State the preparation type.
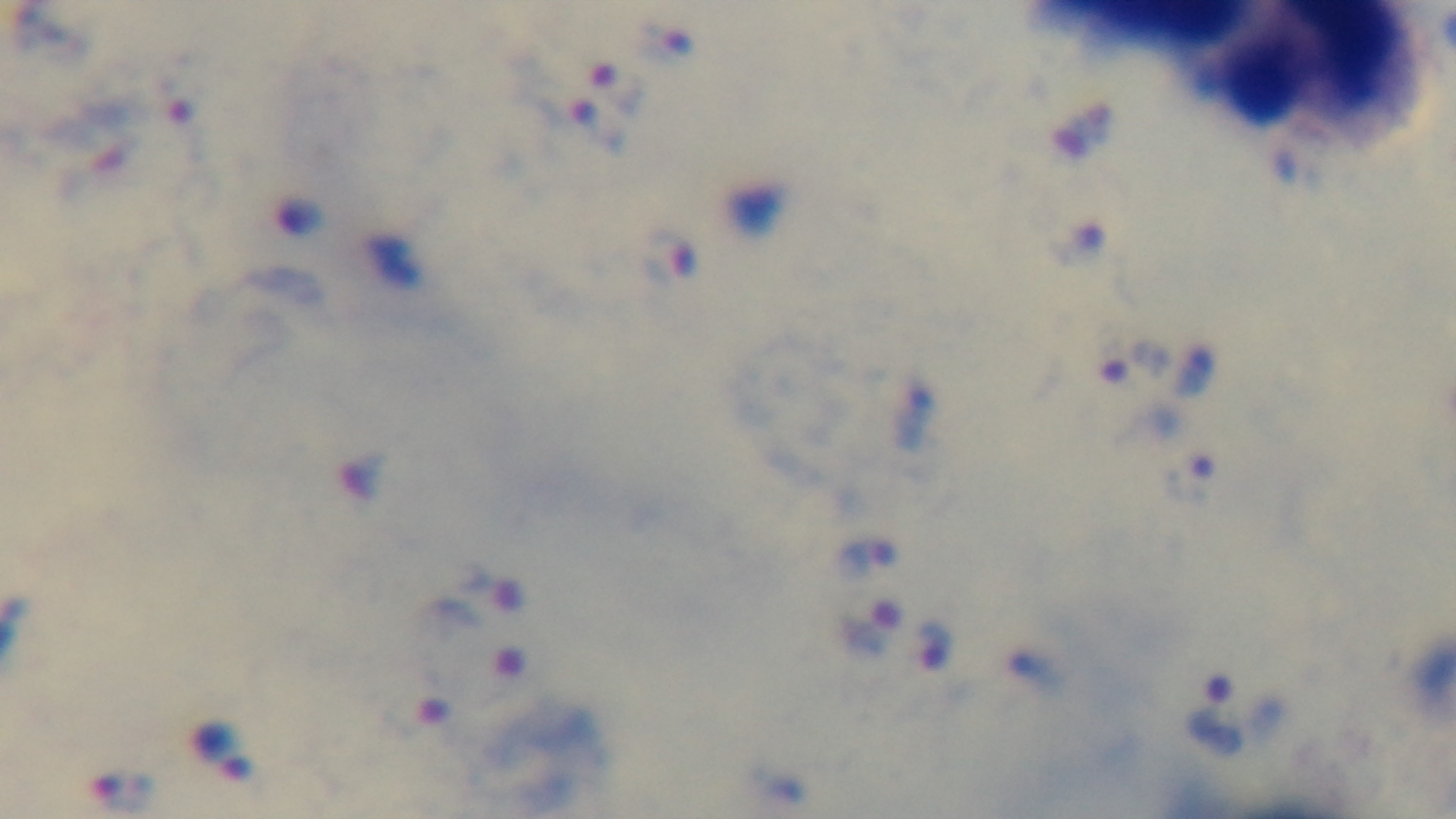
It is a thick blood film.

field of view = single
capture = mounted 4K digital camera
modality = light microscopy
stain = Giemsa
objective = 100x oil immersion
malaria status = positive